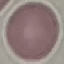
Summary:
  - Malaria status: uninfected
  - Stain: Giemsa
  - Preparation: thin blood film
  - Image type: cell patch, automatically extracted from a larger field of view and resized to 64 × 64 pixels
  - Capture: smartphone camera at the microscope eyepiece